Locate and identify every blood parasite.
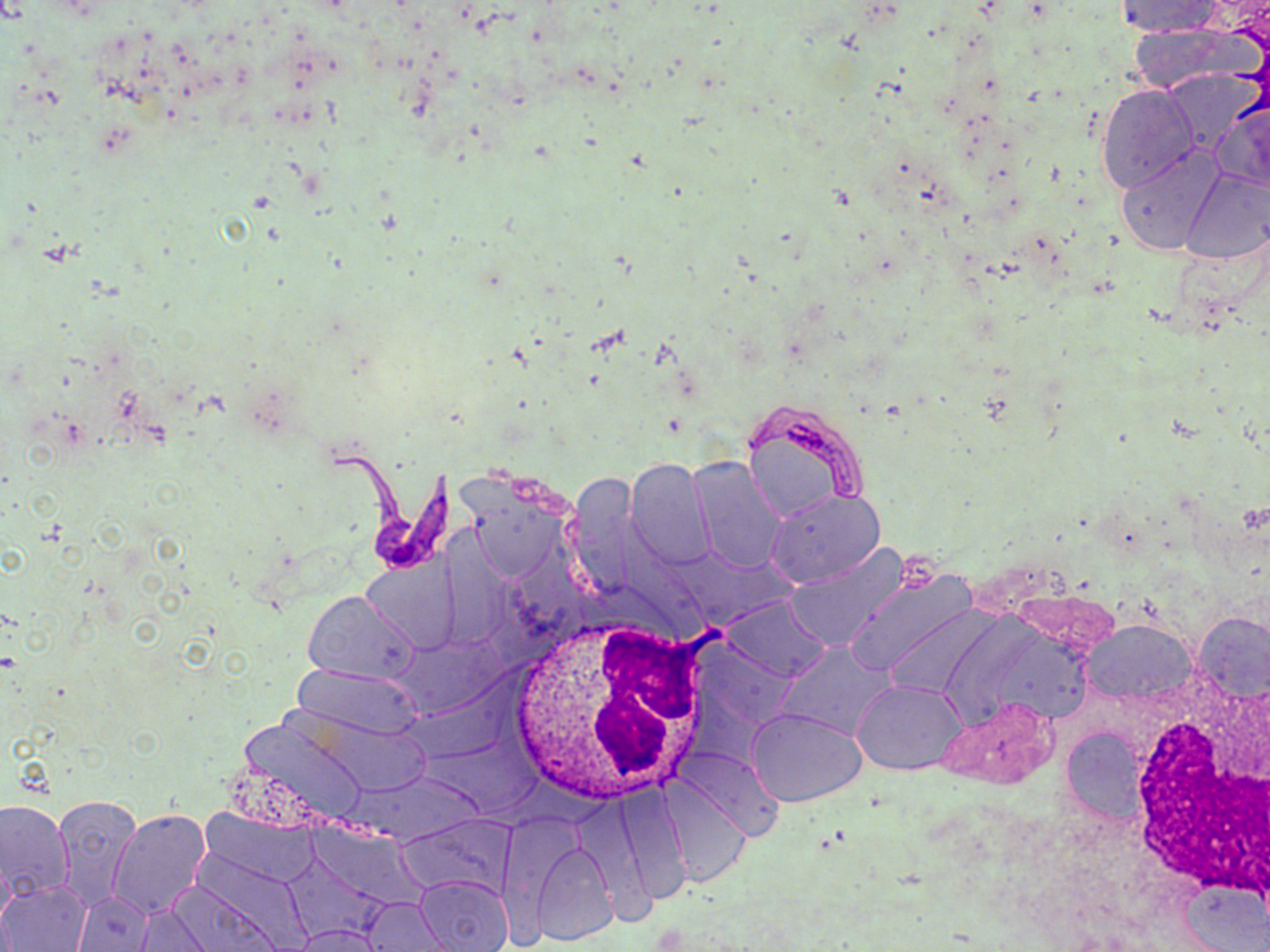
Approximate bounding boxes as [x1, y1, x2, y2] in pixels.
Trypanosoma brucei: [326, 446, 459, 576].
No Plasmodium falciparum, Plasmodium ovale, Plasmodium malariae, Plasmodium vivax, or Babesia divergens observed.

{
  "slide_level_diagnosis": "Trypanosoma brucei",
  "white_blood_cell_locations": "approximate bounding boxes as [x1, y1, x2, y2] in pixels: [510, 616, 716, 802], [1125, 690, 1270, 901]",
  "modality": "optical microscopy",
  "magnification": "1000x",
  "image_size": "1270×952 pixels",
  "uninfected_red_blood_cell_locations": "approximate bounding boxes as [x1, y1, x2, y2] in pixels: [1113, 1, 1226, 38], [1122, 19, 1259, 98], [1161, 70, 1263, 154], [1096, 84, 1199, 193], [1211, 96, 1270, 193], [1114, 145, 1225, 257], [1181, 165, 1270, 266], [689, 459, 786, 574], [625, 460, 717, 571], [765, 488, 885, 587], [784, 546, 916, 655], [843, 568, 978, 683], [303, 589, 419, 685], [722, 596, 831, 681], [1191, 609, 1270, 703], [1084, 621, 1194, 705], [775, 643, 895, 743], [294, 665, 423, 739], [852, 679, 967, 773], [934, 694, 1059, 790], [748, 708, 864, 807], [1060, 727, 1146, 825], [659, 778, 750, 888], [52, 793, 144, 911], [0, 798, 74, 904], [108, 808, 211, 921], [526, 837, 621, 946], [415, 876, 514, 952], [1, 880, 90, 951], [72, 892, 155, 951], [358, 897, 451, 952], [291, 925, 386, 951]",
  "preparation": "thin blood film",
  "stain": "May-Grünwald-Giemsa",
  "field_of_view": "one of a larger specimen"
}